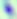
Toxoplasma gondii is seen. Micrograph. 400x magnification.